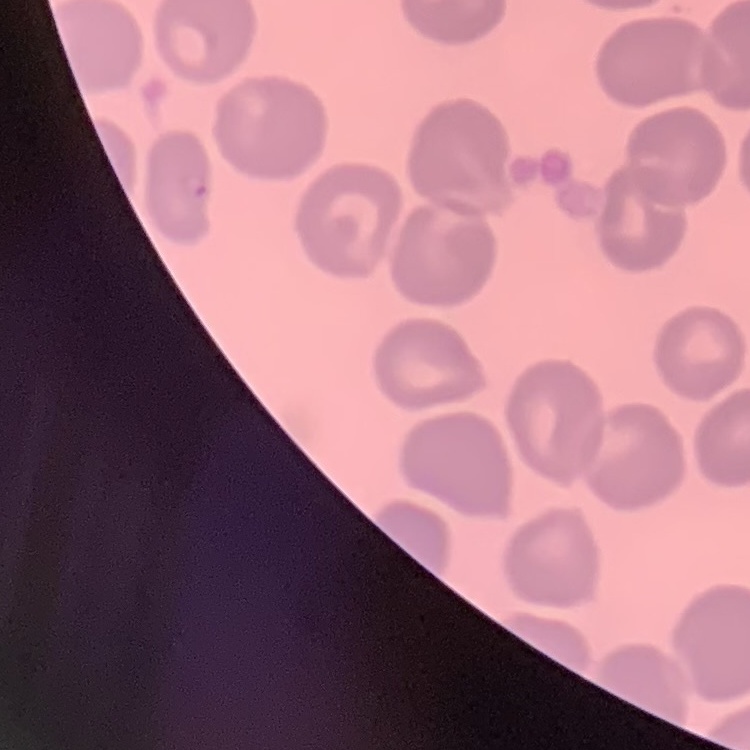

{
  "erythrocyte_morphology": "no rouleaux formation",
  "image_type": "one tile cut from a larger photomicrograph",
  "preparation": "thin blood smear",
  "stain": "Field's or Giemsa"
}